Give the position of every leukocyte visible.
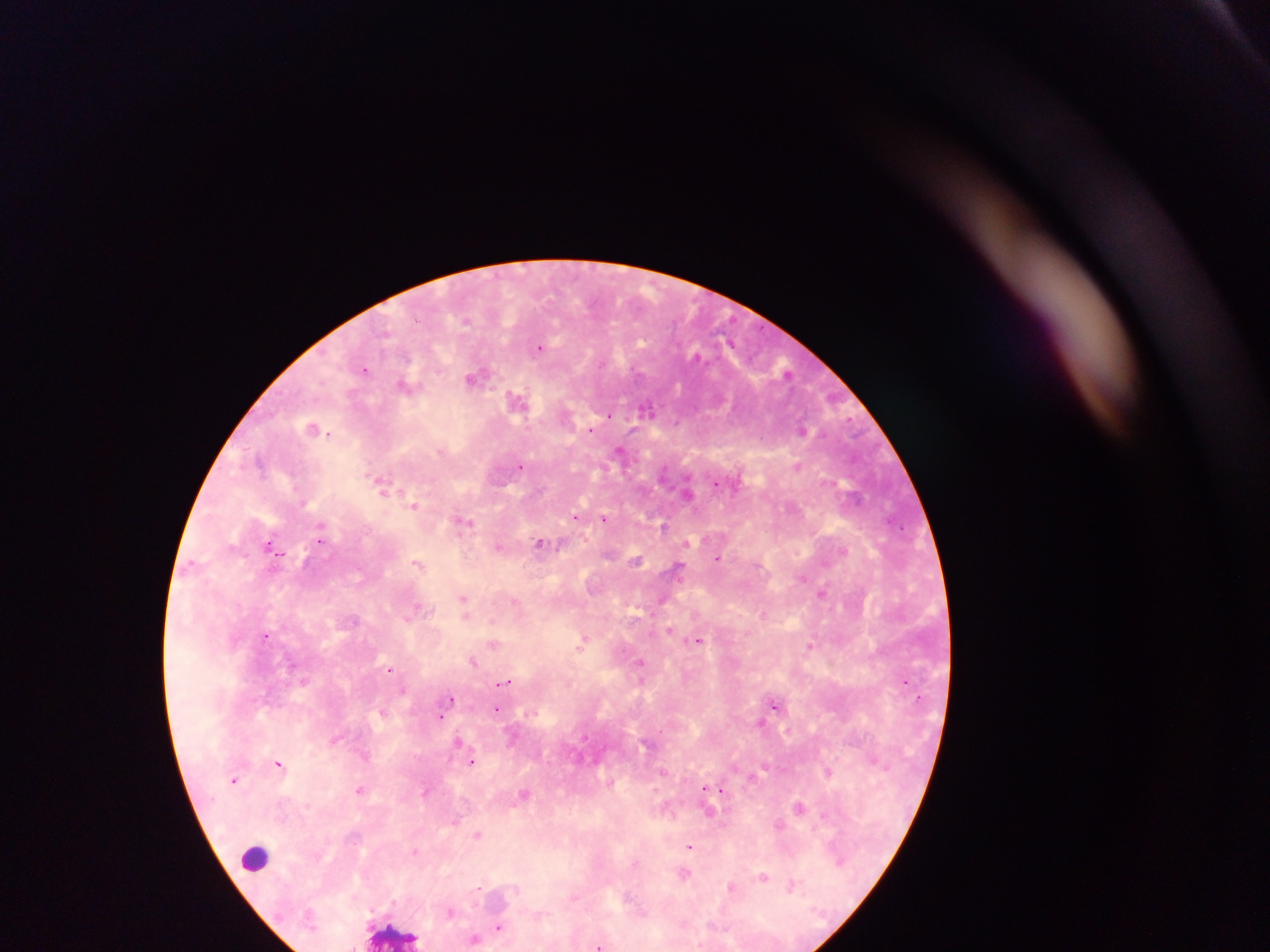
Approximate centers as {x, y} in pixels.
Leukocytes: {255, 858}, {394, 932}.

Summary:
  - Plasmodium parasite locations: {468, 320}, {539, 348}, {695, 356}, {602, 362}, {365, 369}, {475, 376}, {407, 385}, {516, 399}, {647, 407}, {609, 415}, {312, 429}, {590, 429}, {802, 429}, {441, 450}, {621, 450}, {797, 465}, {520, 466}, {717, 484}, {383, 485}, {689, 492}, {414, 505}, {575, 516}, {605, 518}, {464, 521}, {663, 526}, {320, 533}, {320, 540}, {539, 543}, {686, 543}, {270, 545}, {499, 546}, {279, 551}, {843, 551}, {718, 558}, {636, 560}, {416, 563}, {677, 568}, {802, 577}, {822, 593}, {464, 599}, {662, 600}, {515, 602}, {418, 607}, {465, 611}, {763, 613}, {354, 620}, {670, 630}, {265, 636}, {584, 641}, {698, 641}, {493, 644}, {810, 647}, {473, 661}, {641, 662}, {390, 668}, {906, 681}, {504, 682}, {403, 691}, {449, 699}, {775, 704}, {445, 709}, {498, 709}, {382, 711}, {439, 716}, {761, 723}, {335, 739}, {458, 741}, {364, 756}, {472, 761}, {279, 763}, {827, 771}, {235, 780}, {611, 782}, {360, 789}, {704, 789}, {426, 791}, {721, 791}, {523, 794}, {799, 808}, {710, 813}, {824, 816}, {779, 824}, {478, 834}, {690, 847}, {414, 851}, {839, 860}, {685, 874}, {763, 876}, {730, 886}, {792, 886}, {478, 887}, {451, 912}, {499, 927}, {475, 939}, {598, 946}, {353, 947}
  - Image size: 1270×952 pixels
  - Field of view: single
  - Preparation: thick blood film
  - Capture: mobile-phone photograph through a microscope
  - Country: Ghana